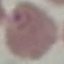

Summary:
  - Malaria status: parasitized
  - Stain: Giemsa
  - Image type: cell patch, automatically extracted from a larger field of view and resized to 64 × 64 pixels
  - Preparation: thin smear
  - Capture: smartphone through the microscope eyepiece